Report the malaria status of this cell.
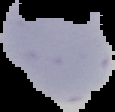
Parasitized.

From a thin blood film. The area outside the segmented cell region is set to black. Image is 115×112 pixels.